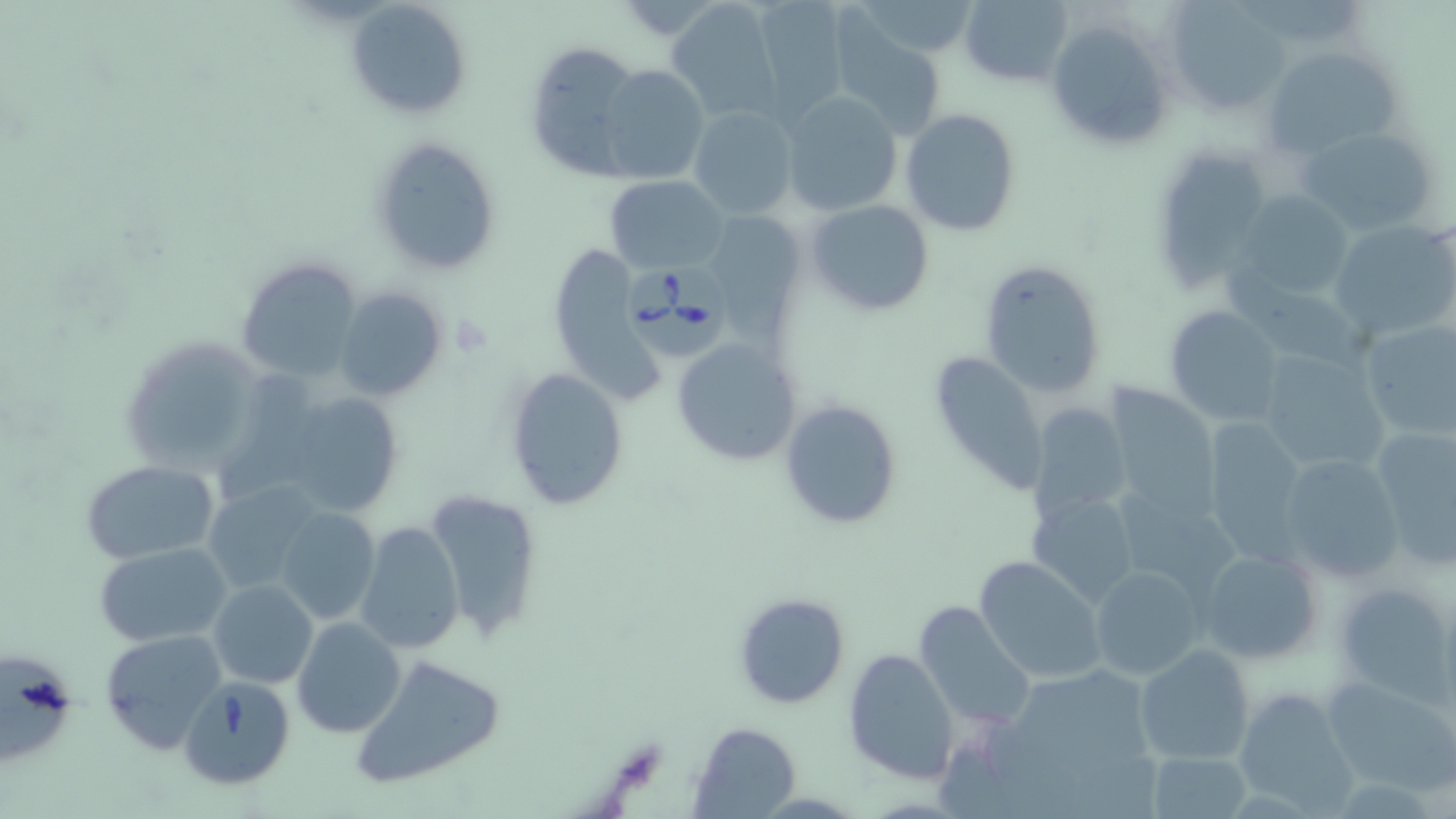
slide_level_diagnosis: Babesia divergens
magnification: 1000x
field_of_view: one of a larger specimen
image_size: 1456×819 pixels
uninfected_red_blood_cell_locations: 'approximate bounding boxes as (x1,y1)-(x2,y2) corner pairs in pixels: (345,0)-(473,120), (749,0)-(850,119), (958,0)-(1073,88), (665,1)-(782,121), (855,1)-(982,59), (1166,1)-(1285,114), (1045,17)-(1177,154), (828,20)-(951,139), (523,39)-(647,179), (1263,46)-(1401,158), (593,63)-(710,185), (779,92)-(903,217), (687,105)-(798,220), (900,108)-(1022,237), (1298,124)-(1442,235), (368,136)-(502,276), (1152,148)-(1265,296), (604,176)-(728,273), (1232,189)-(1357,300), (805,200)-(935,316), (700,212)-(806,336), (1329,220)-(1456,342), (550,244)-(668,409), (237,255)-(364,383), (979,259)-(1108,399), (335,287)-(447,403), (1163,306)-(1284,427), (1355,320)-(1456,444), (117,335)-(268,475), (672,338)-(804,466), (1255,348)-(1391,476), (929,351)-(1052,489), (505,366)-(627,509), (1102,385)-(1221,518), (280,391)-(405,520), (778,398)-(904,531), (1026,402)-(1132,521), (1200,418)-(1309,563), (1369,425)-(1455,569), (1275,452)-(1406,584), (80,459)-(220,564), (202,478)-(324,592), (424,488)-(544,641), (1114,489)-(1242,600), (1028,490)-(1141,607), (276,507)-(380,626), (355,520)-(464,654), (93,542)-(232,648), (1199,545)-(1325,666), (974,555)-(1107,684), (1093,566)-(1206,679), (209,578)-(318,689), (1334,580)-(1456,699), (732,592)-(852,709), (912,601)-(1036,731), (292,617)-(407,738), (101,627)-(230,754), (1135,643)-(1255,766), (843,648)-(961,781), (0,651)-(75,768), (348,655)-(507,790), (1321,676)-(1455,793), (1234,690)-(1357,815), (688,723)-(802,817), (1147,750)-(1252,817)'
preparation: thin blood film
stain: May-Grünwald-Giemsa
babesia_divergens_infected_red_blood_cell_locations: 'approximate bounding boxes as (x1,y1)-(x2,y2) corner pairs in pixels: (623,255)-(734,356), (179,675)-(296,791)'
modality: optical microscopy